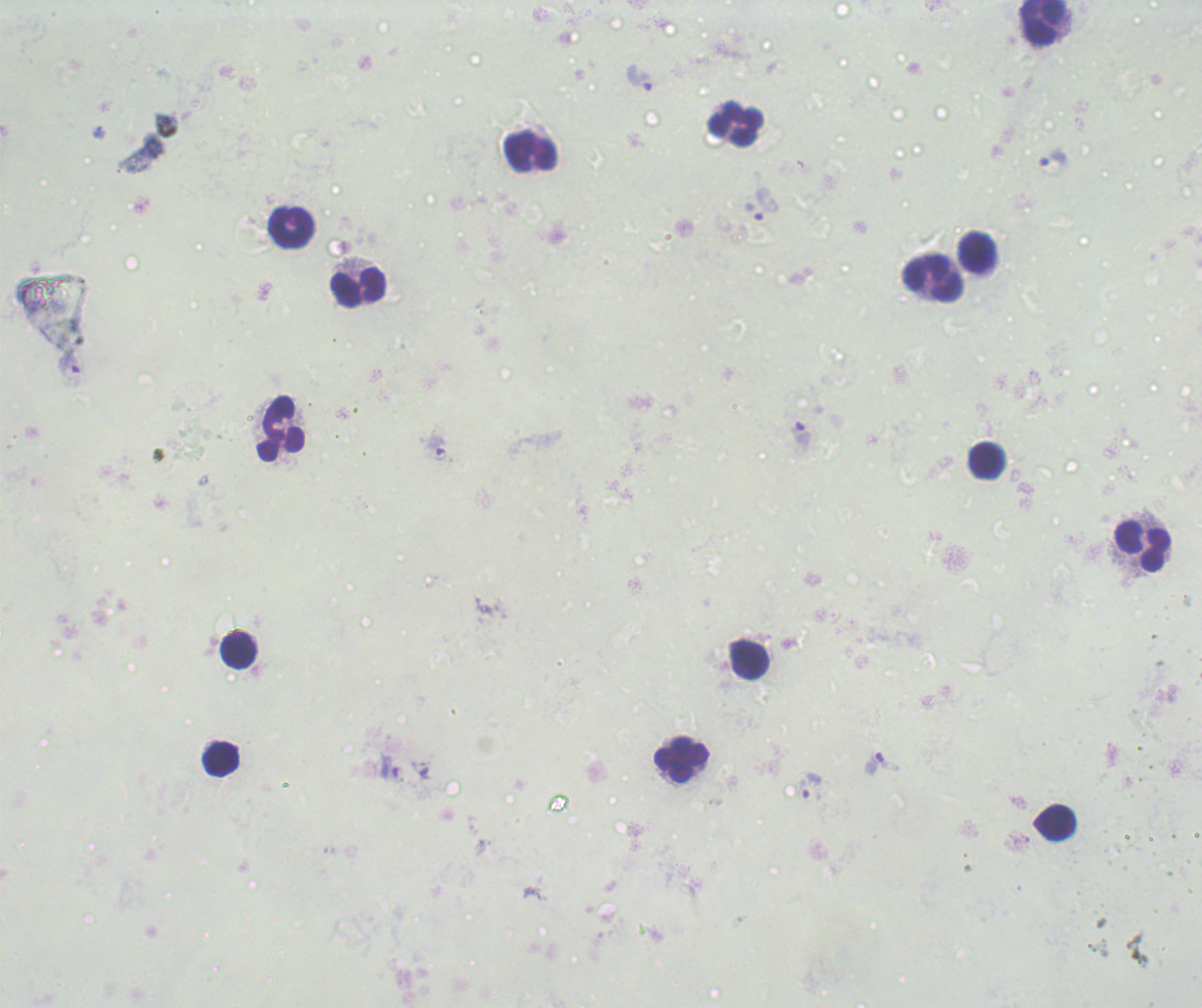
Approximate centers as [x, y] in pixels. Leukocyte locations: [1042, 22], [735, 123], [531, 152], [292, 227], [977, 252], [933, 277], [359, 287], [281, 429], [801, 434], [986, 460], [1142, 546], [238, 650], [749, 659], [221, 760], [681, 761], [1055, 822]. Trophozoite locations: [639, 77], [1053, 159], [765, 204], [436, 447], [882, 763], [389, 767], [810, 785]. Result: malaria parasites identified. Romanowsky stain. Background quality: unsatisfactory. Single field of view. Previously used in a real diagnosis. Captured at 100x magnification. Image is 1202×1008 pixels. Thick blood smear.